Describe the morphology of the erythrocytes.
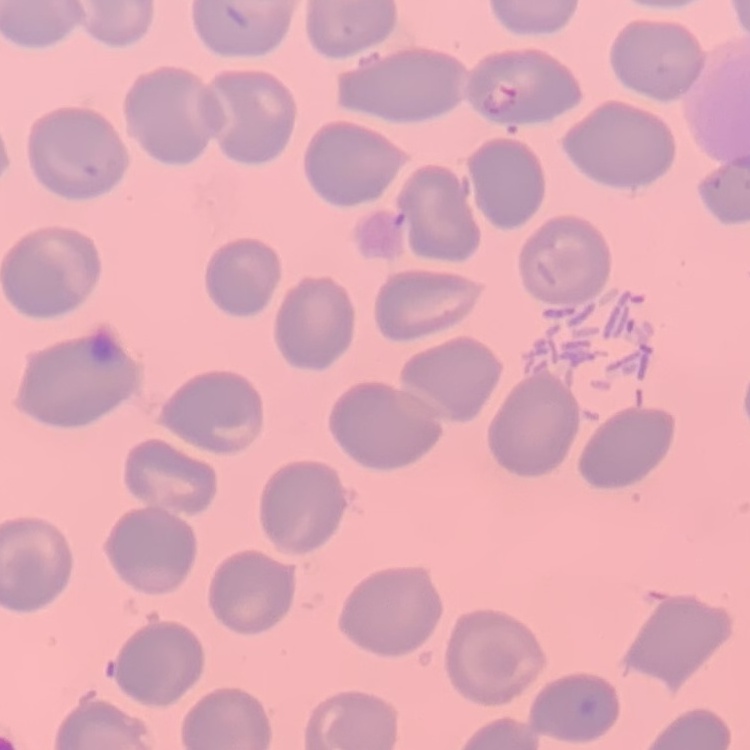
They show no rouleaux formation.

{
  "preparation": "thin blood film",
  "image_type": "one tile cut from a larger photomicrograph",
  "stain": "Field's or Giemsa"
}